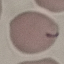
Summary:
  - Malaria status: uninfected
  - Capture: smartphone camera at the microscope eyepiece
  - Image type: cell patch, automatically extracted from a larger field of view and resized to 64 × 64 pixels
  - Preparation: thin smear
  - Stain: Giemsa